Classify this cell by malaria status.
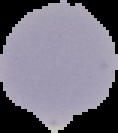
Uninfected.

Cell region segmented out of the field of view; the surrounding area is masked to black. From a thin blood film. Image is 118×133 pixels.